Assess this cell for malaria.
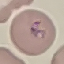

It is parasitized.

preparation = thin smear
image type = cell patch, automatically extracted from a larger field of view and resized to 64 × 64 pixels
capture = smartphone through the microscope eyepiece
stain = Giemsa